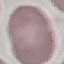

Result: negative for malaria parasites. Thin blood smear. Giemsa stain. Photographed with a smartphone camera at the microscope eyepiece. Cell patch, automatically extracted from a larger field of view and resized to 64 × 64 pixels.